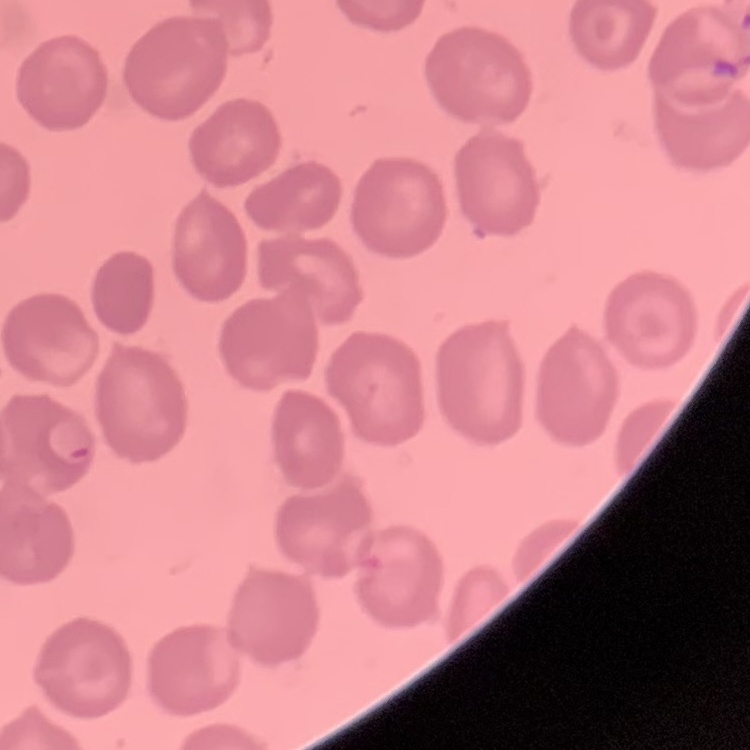
Summary:
  - Red blood cell morphology: no rouleaux formation
  - Image type: one tile cut from a larger photomicrograph
  - Preparation: thin blood smear
  - Stain: Field's or Giemsa